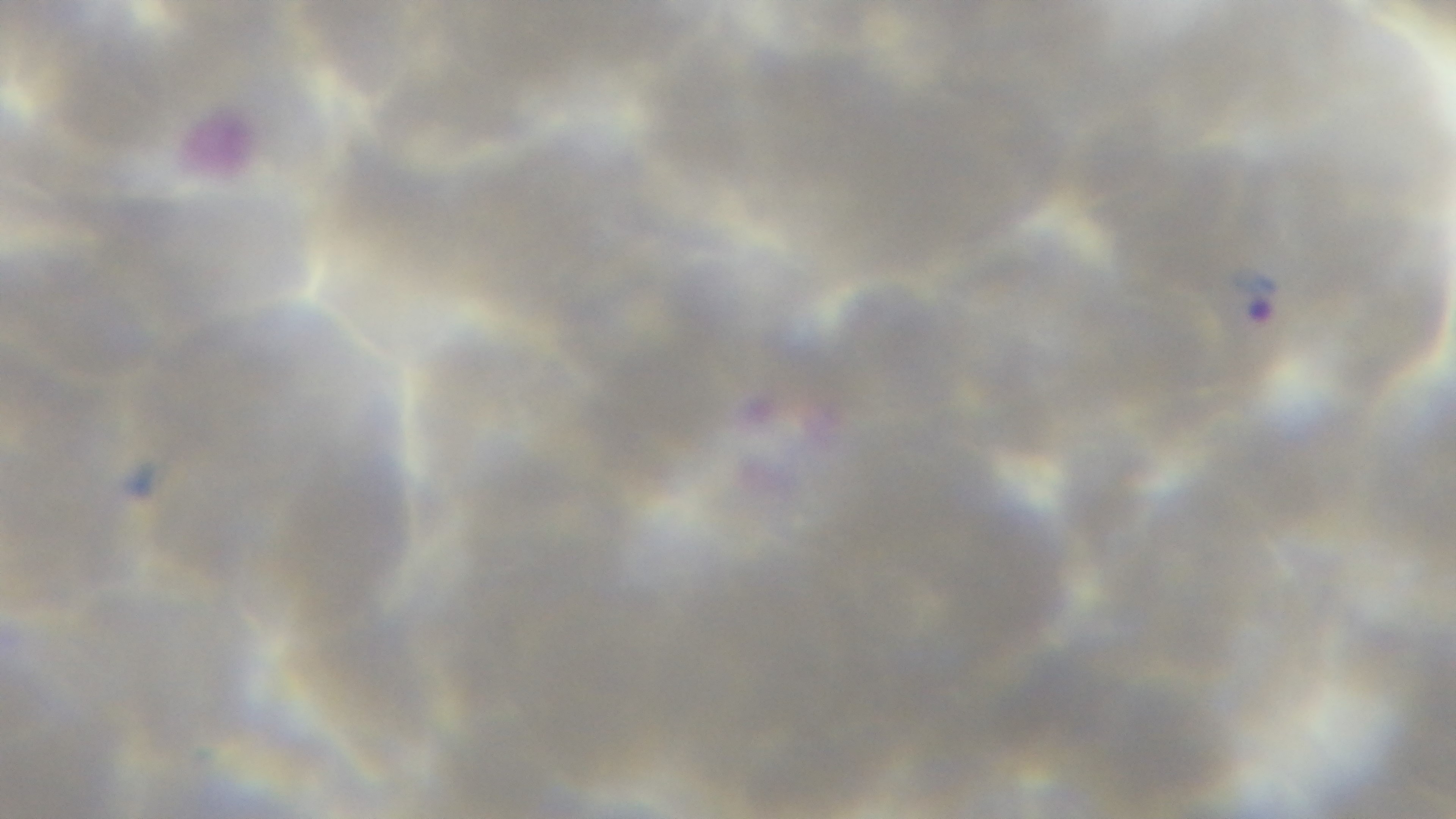

Summary:
  - Preparation: thin blood film
  - Modality: light microscopy
  - Stain: Giemsa
  - Objective: 100x oil immersion
  - Field of view: one from the slide
  - Malaria status: infected
  - Capture: mounted 4K digital camera